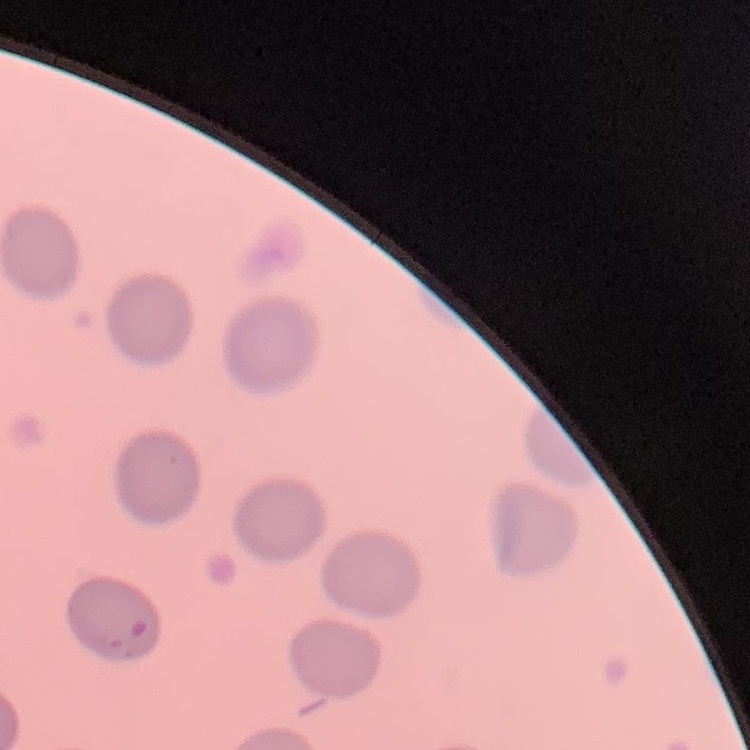

red_blood_cell_morphology: no rouleaux formation
image_type: square crop of a larger photomicrograph
stain: Field's or Giemsa
preparation: thin blood smear